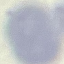
Result: no malaria parasites seen. Thin blood film. Cell patch, automatically extracted from a larger field of view and resized to 64 × 64 pixels. Acquired by smartphone through the microscope eyepiece. Giemsa stain.